Point out each Plasmodium parasite.
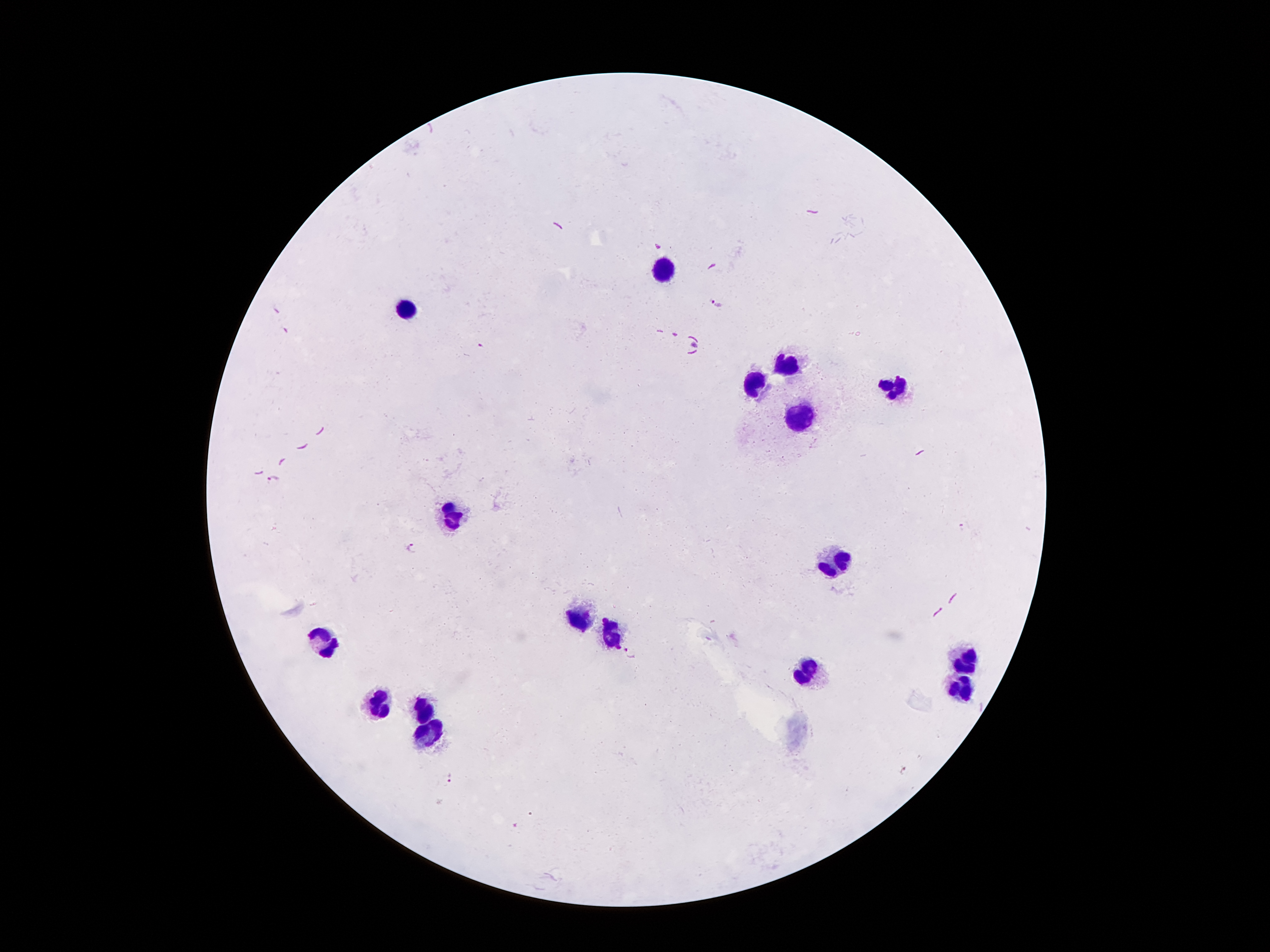
Approximate centers as (x, y) in pixels.
Plasmodium parasites: (717, 303), (694, 344), (481, 345), (274, 480), (412, 548), (629, 653), (905, 770), (450, 780), (514, 825).

Leukocyte locations: (661, 273), (409, 305), (787, 364), (898, 384), (755, 386), (799, 421), (453, 505), (839, 562), (584, 618), (611, 633), (327, 638), (965, 658), (809, 673), (962, 685), (376, 702), (423, 710), (431, 739). Image is 1270×952 pixels. One field from this slide. Giemsa stain. Patient malaria status: positive for Plasmodium falciparum. Smartphone photograph taken through the microscope eyepiece. 100x magnification. Thick blood smear.